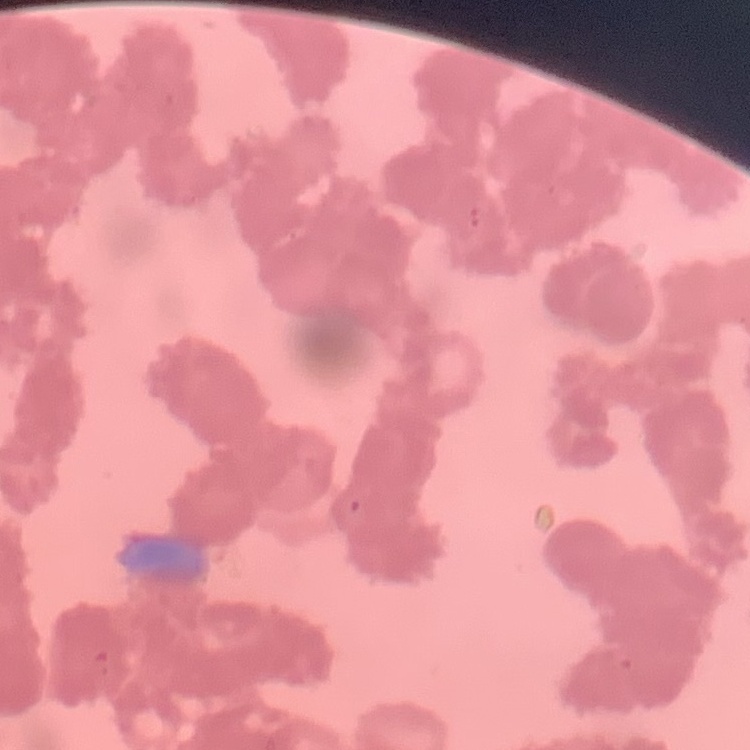

red blood cell morphology = rouleaux formation
image type = square crop of a larger photomicrograph
stain = Field's or Giemsa
preparation = thin blood film